Locate every parasitized red blood cell.
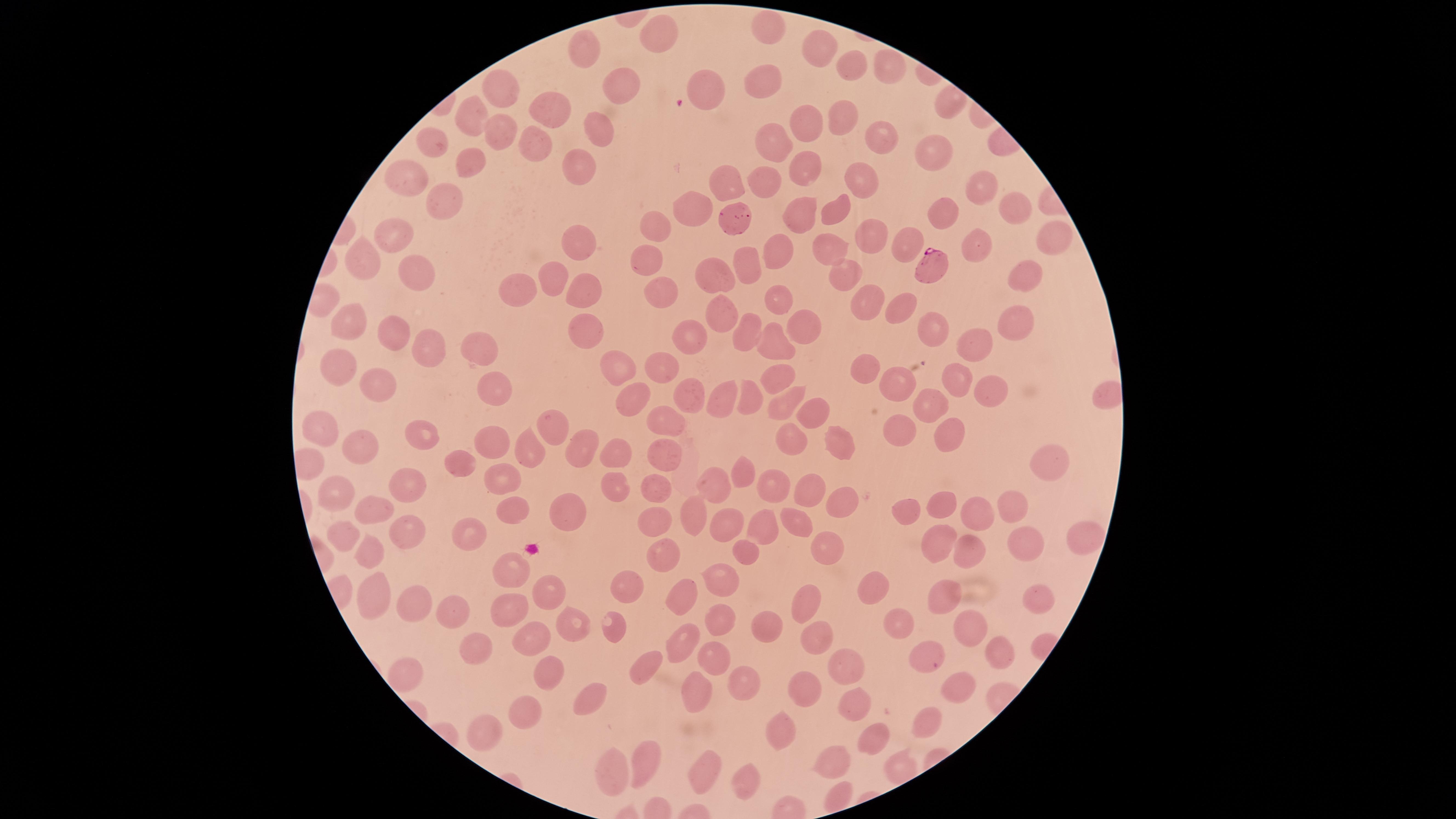

Approximate marker points as (x, y) in pixels.
Parasitized red blood cells: (934, 263).

Approximate marker points as (x, y) in pixels. Uninfected red blood cells: (768, 31), (656, 36), (816, 50), (580, 55), (848, 66), (887, 66), (767, 78), (626, 86), (491, 88), (554, 103), (844, 112), (470, 114), (600, 128), (882, 128), (505, 133), (804, 133), (434, 141), (536, 142), (922, 146), (775, 149), (472, 166), (585, 166), (798, 166), (409, 180), (983, 181), (864, 182), (765, 185), (725, 186), (441, 202), (1012, 202), (835, 207), (791, 210), (691, 215), (942, 217), (735, 221), (1051, 226), (655, 227), (393, 233), (874, 235), (905, 241), (578, 245), (978, 246), (832, 250), (781, 253), (362, 261), (649, 264), (747, 267), (411, 271), (843, 272), (1025, 274), (713, 276), (557, 277), (661, 291), (518, 292), (582, 293), (773, 302), (866, 302), (900, 309), (714, 317), (352, 324), (938, 325), (1020, 325), (802, 328), (391, 332), (582, 332), (749, 340), (692, 344), (776, 346), (977, 347), (483, 353), (420, 355), (660, 363), (340, 369), (615, 369), (859, 369), (776, 377), (953, 378), (493, 383), (901, 383), (376, 384), (993, 389), (686, 394), (747, 397), (721, 398), (940, 400), (627, 403), (782, 406), (808, 413), (665, 420), (321, 427), (550, 428), (895, 428), (426, 433), (945, 435), (491, 436), (791, 439), (835, 441), (366, 449), (575, 450), (531, 451), (610, 455), (663, 455), (462, 459), (1049, 463), (745, 473), (710, 479), (401, 482), (499, 483), (768, 486), (608, 489), (660, 490), (812, 490), (335, 491), (840, 500), (939, 504), (1012, 505), (562, 511), (688, 511), (907, 511), (374, 512), (514, 512), (975, 513), (653, 520), (726, 520), (797, 523), (400, 526), (759, 527), (1085, 531), (348, 533), (941, 539), (1028, 539), (470, 540), (743, 547), (971, 548), (369, 550), (662, 552), (826, 553), (500, 568), (722, 582), (630, 586), (370, 589), (548, 591), (866, 591), (943, 592), (682, 596), (1037, 597), (406, 599), (805, 600), (508, 611), (447, 613), (723, 615), (569, 621), (896, 625), (768, 628), (971, 628), (811, 632), (614, 635), (541, 637), (679, 638), (478, 646), (923, 649), (998, 650), (714, 653), (648, 661), (410, 669), (845, 669), (539, 670), (737, 682), (697, 686), (803, 688), (957, 688), (590, 696), (852, 705), (525, 714), (925, 721), (779, 726), (478, 730), (869, 738), (641, 760), (827, 760), (613, 768), (703, 768), (743, 778). Image is 1456×819 pixels. Photographed with a smartphone camera through the microscope eyepiece. Species: Plasmodium falciparum. Circular visible region. Giemsa-stained preparation. One field of view of the specimen. Thin smear of blood.